Comment on the morphology of the red blood cells.
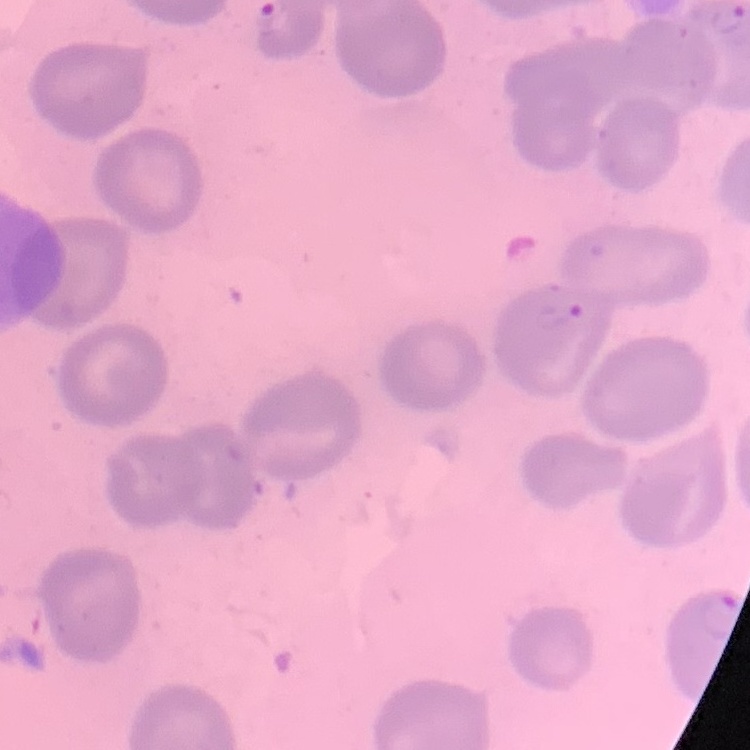
They show no rouleaux formation.

Summary:
  - Stain: Field's or Giemsa
  - Preparation: thin peripheral smear
  - Image type: one tile cut from a larger photomicrograph